Outline each blood parasite and name the species.
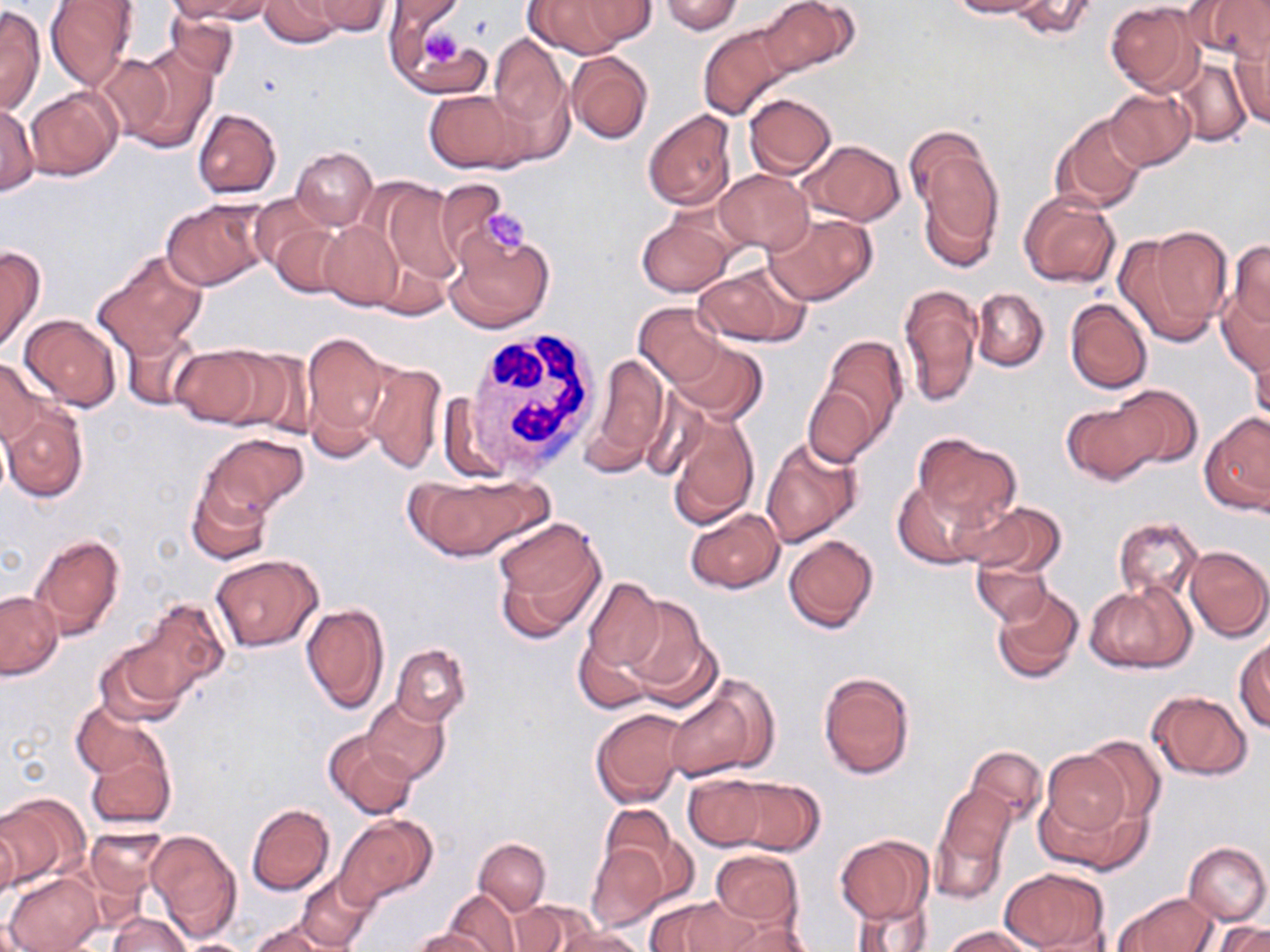

No blood parasites observed.

Summary:
  - Coordinate format: approximate bounding boxes as (x1,y1)-(x2,y2) corner pairs in pixels
  - Platelet locations: (414,22)-(471,75), (476,205)-(534,254)
  - Uninfected red blood cell locations: (167,0)-(267,22), (260,0)-(344,48), (312,0)-(392,36), (387,0)-(464,37), (525,0)-(634,57), (570,0)-(658,48), (658,0)-(744,35), (946,0)-(1049,18), (1008,0)-(1098,40), (1187,0)-(1270,63), (44,1)-(138,90), (758,1)-(857,79), (1105,2)-(1202,96), (0,4)-(45,115), (165,9)-(239,80), (384,14)-(472,83), (698,22)-(794,119), (488,33)-(568,129), (1230,37)-(1270,130), (113,43)-(219,154), (565,52)-(653,145), (1171,58)-(1252,145), (26,87)-(122,180), (424,87)-(528,173), (1104,88)-(1196,171), (743,94)-(837,177), (0,101)-(40,195), (192,109)-(281,198), (643,110)-(738,213), (1051,113)-(1148,214), (908,132)-(1004,266), (799,139)-(905,226), (290,146)-(377,230), (714,169)-(812,254), (375,179)-(464,289), (1018,192)-(1120,289), (160,199)-(269,290), (253,201)-(340,295), (764,210)-(876,306), (636,214)-(735,296), (317,220)-(404,310), (1117,227)-(1232,347), (443,228)-(555,334), (1227,241)-(1270,331), (0,245)-(44,353), (93,251)-(208,359), (695,263)-(808,346), (898,283)-(982,408), (1216,286)-(1270,378), (972,288)-(1049,370), (1065,299)-(1153,394), (633,304)-(726,385), (19,313)-(122,410), (119,327)-(201,411), (302,332)-(392,449), (813,334)-(910,453), (1247,337)-(1269,433), (668,339)-(766,422), (168,344)-(270,427), (214,346)-(313,435), (590,353)-(669,467), (0,356)-(44,447), (360,358)-(445,474), (803,381)-(880,468), (1108,384)-(1204,472), (1062,396)-(1166,485), (1,405)-(88,503), (665,409)-(758,527), (1200,412)-(1270,516), (199,433)-(309,520), (912,433)-(1020,527), (760,437)-(863,547), (403,471)-(554,565), (893,478)-(993,569), (186,479)-(271,565), (960,499)-(1069,577), (686,509)-(784,593), (490,516)-(605,638), (1114,516)-(1203,600), (30,533)-(126,640), (783,534)-(878,634), (1184,545)-(1269,641), (210,555)-(322,651), (970,555)-(1054,627), (581,578)-(666,674), (991,584)-(1084,684), (1085,584)-(1193,674), (1,591)-(62,680), (618,595)-(712,702), (130,598)-(230,701), (301,603)-(390,714), (573,636)-(654,713), (1234,637)-(1270,732), (95,640)-(191,725), (391,644)-(470,725), (819,672)-(914,779), (664,679)-(775,781), (1147,689)-(1253,780), (363,696)-(450,783), (72,699)-(162,779), (590,708)-(689,807), (325,731)-(420,820), (1076,736)-(1167,829), (85,743)-(176,830), (965,744)-(1047,826), (1038,748)-(1135,847), (684,774)-(768,851), (722,777)-(825,855), (932,785)-(1015,902), (0,792)-(87,887), (246,803)-(335,896), (600,803)-(687,897), (335,814)-(436,906), (0,822)-(19,906), (85,826)-(167,902), (145,830)-(241,941), (834,834)-(933,924), (474,838)-(550,915), (585,842)-(670,932), (1184,842)-(1269,925), (710,850)-(804,929), (999,867)-(1110,951), (4,873)-(101,952), (296,873)-(377,952), (446,890)-(521,951), (849,892)-(935,952), (1115,892)-(1217,952), (644,897)-(743,952), (511,901)-(595,951), (108,912)-(191,952), (712,917)-(816,952), (1218,921)-(1270,952), (249,922)-(337,951), (941,926)-(1037,952), (412,927)-(496,952), (553,927)-(647,952), (171,938)-(258,952)
  - White blood cell locations: (458,327)-(605,482)
  - Slide-level diagnosis: no evidence of blood parasites
  - Field of view: single
  - Modality: light microscopy
  - Image size: 1270×952 pixels
  - Magnification: 1000x
  - Stain: May-Grünwald-Giemsa
  - Preparation: thin blood smear